Locate every Plasmodium parasite and every leukocyte.
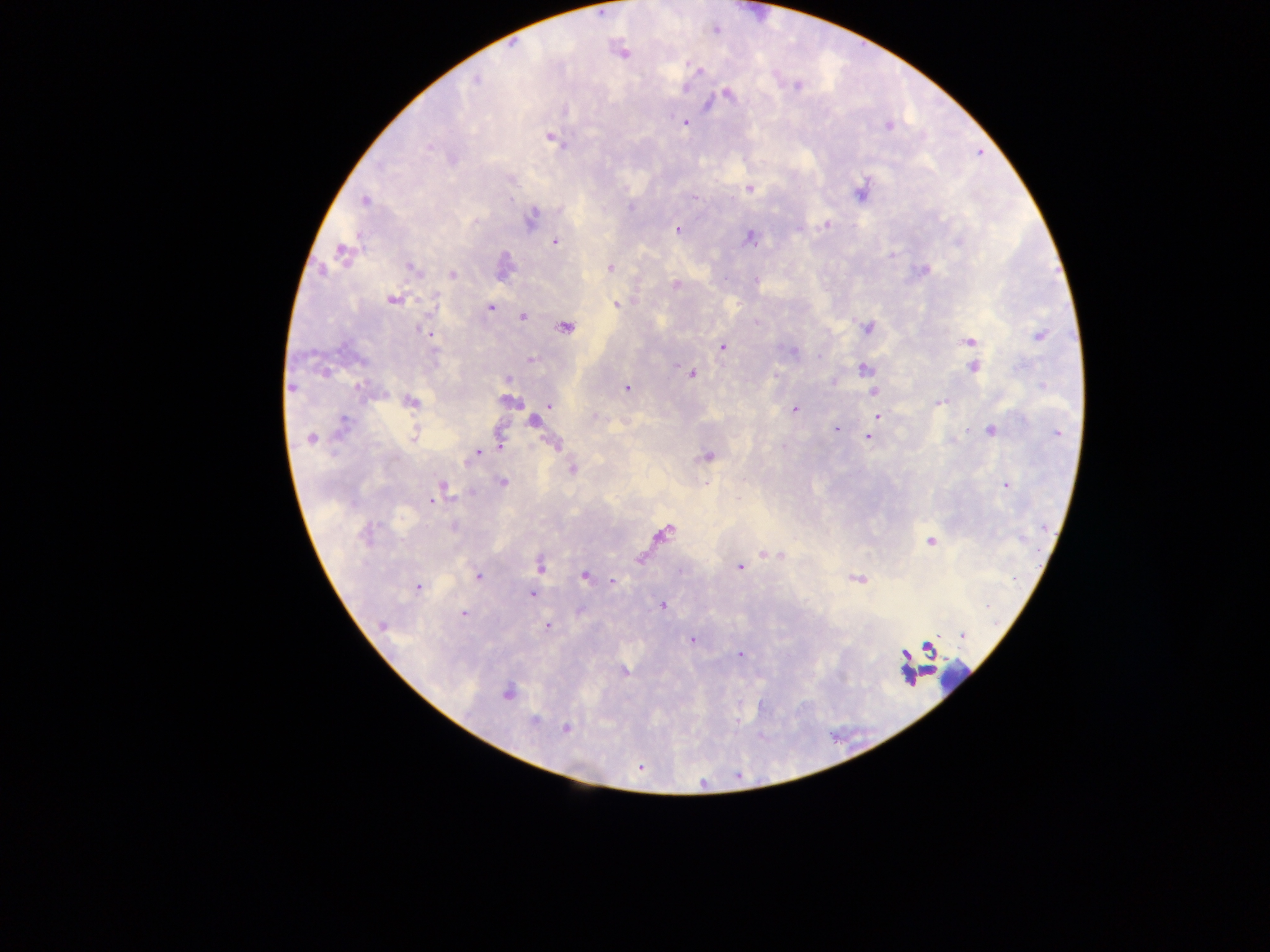
Approximate centers as x y in pixels.
Plasmodium parasites: 622 52; 698 70; 475 80; 797 85; 726 93; 684 122; 888 124; 550 137; 750 188; 861 189; 365 200; 530 217; 827 224; 678 230; 750 237; 555 241; 341 252; 892 254; 503 266; 410 268; 609 268; 923 270; 452 274; 755 281; 676 284; 392 299; 616 303; 489 307; 522 316; 866 326; 564 327; 427 333; 1040 335; 969 342; 722 346; 530 359; 973 366; 863 368; 692 373; 506 378; 291 387; 627 387; 873 390; 409 401; 508 401; 940 403; 549 405; 794 409; 878 415; 533 421; 836 429; 989 430; 1057 432; 413 436; 869 436; 310 438; 500 440; 554 444; 477 453; 707 455; 572 468; 502 481; 1006 485; 440 489; 433 500; 666 530; 931 541; 765 554; 780 554; 540 564; 739 567; 585 575; 478 576; 856 578; 611 581; 417 587; 532 593; 662 605; 463 613; 383 625; 547 626; 962 636; 692 639; 929 648; 740 654; 623 671; 506 692; 533 721; 565 728; 639 767.
Leukocytes: 928 650; 911 669; 955 677.

Collected in Ghana. Image is 1270×952 pixels. Thick blood film. Photographed through a microscope with a mobile-phone camera. One field of view.